Describe the morphology of the red blood cells.
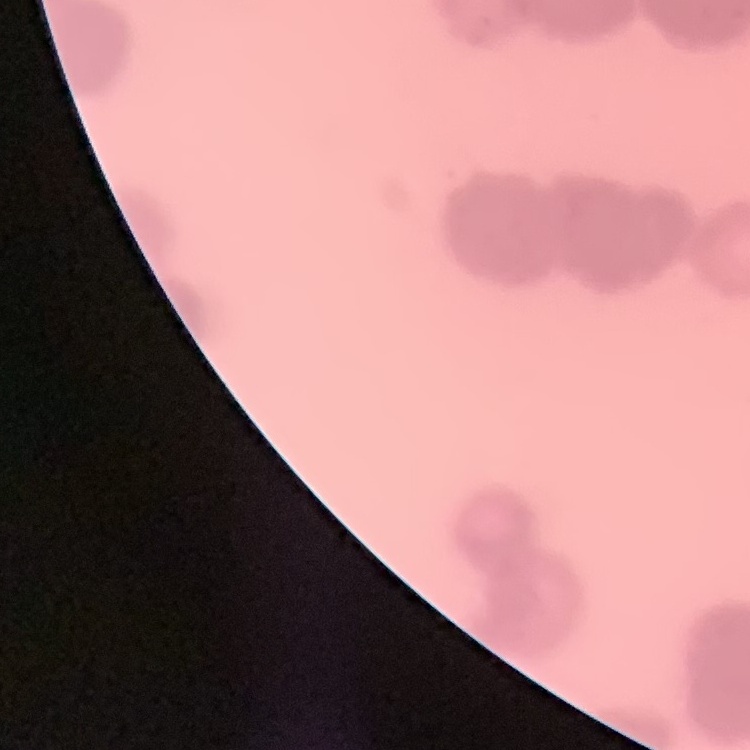

They show rouleaux formation.

stain = Field's or Giemsa
preparation = thin blood film
image type = square crop of a larger photomicrograph